Name the parasite shown.
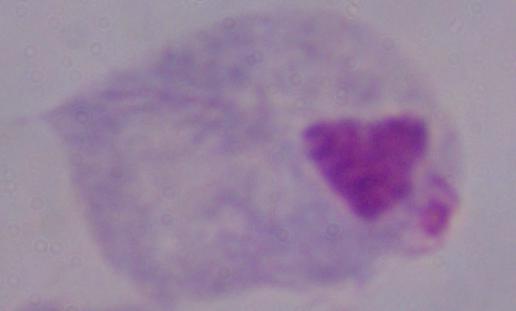

A trichomonad.

Summary:
  - Magnification: 1000x
  - Modality: photomicrograph